Locate and identify every blood parasite.
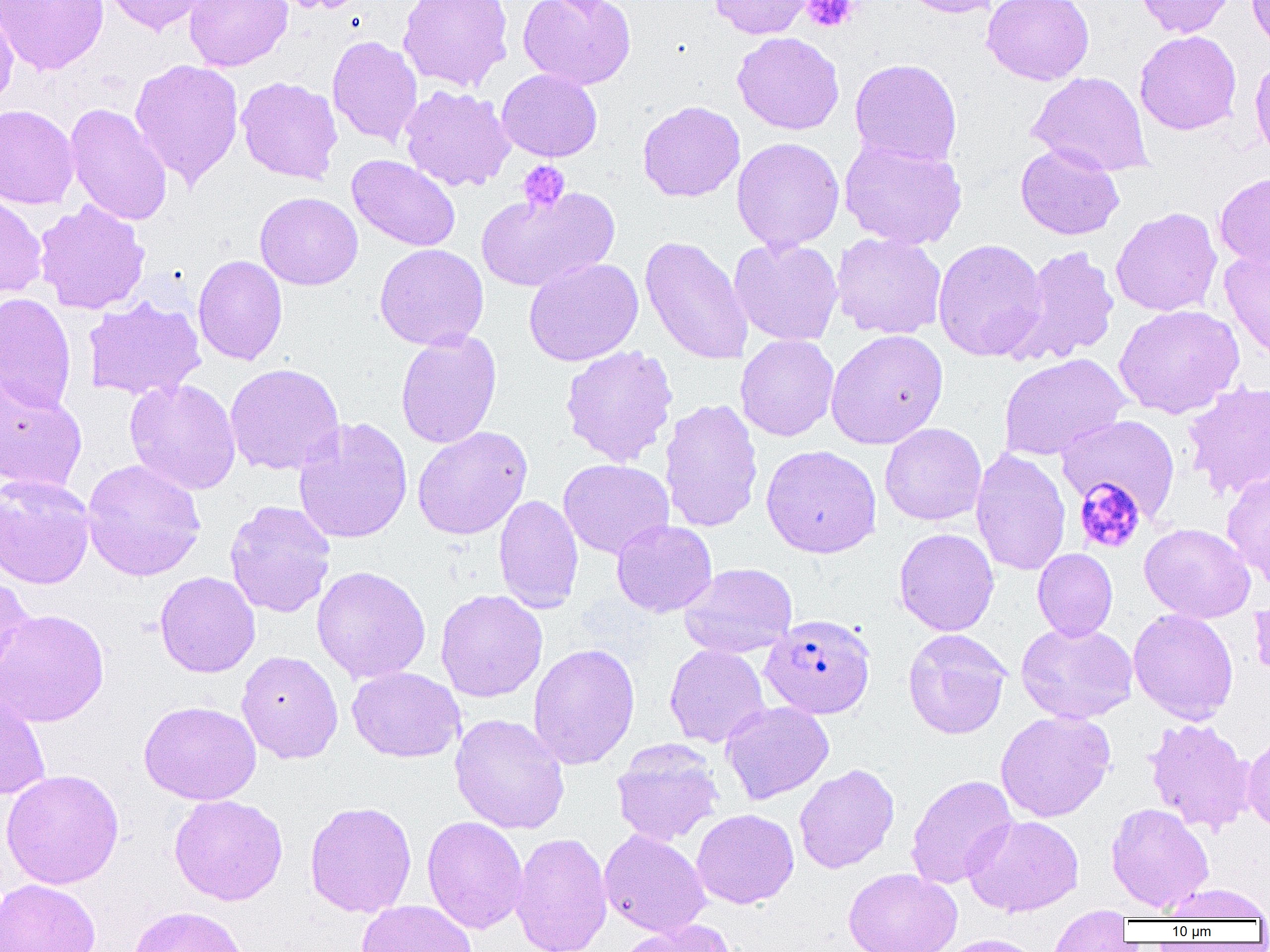

Approximate bounding boxes as (x1, y1, x2, y2) in pixels.
Plasmodium falciparum-infected red blood cells: (761, 613, 876, 719).
No Plasmodium ovale, Plasmodium malariae, Plasmodium vivax, Babesia divergens, or Trypanosoma brucei observed.

Platelet locations: (801, 0, 860, 32), (517, 160, 570, 212), (1074, 478, 1145, 553). Uninfected red blood cell locations: (0, 0, 109, 75), (101, 0, 213, 36), (184, 0, 292, 71), (270, 0, 371, 14), (398, 0, 513, 92), (518, 0, 636, 90), (708, 0, 815, 39), (896, 0, 1005, 18), (982, 0, 1094, 85), (1132, 0, 1237, 38), (1247, 0, 1270, 56), (0, 6, 18, 113), (1134, 30, 1242, 135), (733, 32, 845, 135), (327, 35, 422, 146), (1250, 55, 1270, 165), (129, 58, 244, 188), (849, 58, 963, 167), (496, 68, 602, 162), (1027, 71, 1153, 176), (236, 76, 343, 184), (400, 85, 515, 192), (637, 100, 745, 202), (65, 103, 172, 226), (0, 104, 79, 209), (731, 137, 845, 253), (839, 138, 968, 250), (1015, 143, 1124, 240), (347, 154, 460, 252), (1215, 172, 1270, 270), (476, 186, 619, 292), (0, 191, 47, 301), (254, 191, 363, 290), (34, 200, 151, 315), (1111, 207, 1222, 316), (832, 232, 947, 339), (640, 235, 754, 365), (728, 237, 843, 347), (932, 238, 1047, 362), (374, 243, 489, 351), (1011, 245, 1120, 365), (1220, 248, 1270, 363), (193, 254, 288, 366), (523, 257, 644, 367), (0, 292, 77, 413), (82, 295, 206, 400), (1113, 304, 1244, 419), (825, 329, 948, 450), (395, 330, 502, 449), (735, 334, 839, 441), (559, 345, 679, 467), (998, 353, 1131, 461), (224, 363, 345, 476), (0, 371, 87, 495), (124, 378, 242, 495), (1181, 380, 1270, 500), (659, 399, 764, 533), (1057, 415, 1180, 519), (293, 417, 413, 545), (879, 423, 987, 526), (412, 426, 532, 540), (760, 444, 882, 558), (970, 448, 1071, 576), (81, 459, 206, 581), (558, 459, 674, 559), (1221, 469, 1270, 588), (0, 474, 96, 590), (493, 493, 583, 613), (224, 500, 336, 618), (611, 520, 717, 617), (1139, 522, 1255, 623), (894, 527, 999, 636), (1032, 548, 1118, 641), (678, 563, 797, 659), (311, 565, 431, 684), (154, 571, 260, 678), (0, 573, 34, 688), (435, 589, 548, 703), (1250, 594, 1270, 682), (0, 608, 109, 728), (1128, 609, 1239, 724), (1016, 621, 1138, 724), (902, 628, 1011, 739), (528, 642, 640, 770), (664, 643, 771, 748), (236, 650, 343, 764), (347, 666, 465, 762), (0, 690, 51, 800), (138, 700, 261, 805), (720, 701, 834, 805), (995, 710, 1115, 822), (449, 713, 570, 834), (1144, 717, 1255, 835), (1243, 732, 1270, 834), (612, 740, 724, 846), (794, 763, 899, 874), (0, 768, 124, 889), (906, 774, 1018, 889), (168, 794, 288, 905), (304, 801, 417, 917), (1106, 802, 1214, 912), (692, 808, 799, 909), (963, 814, 1084, 917), (422, 816, 528, 935), (599, 829, 711, 938), (511, 831, 613, 952), (843, 867, 962, 952), (0, 879, 101, 952), (1162, 883, 1270, 921), (356, 900, 477, 952), (128, 905, 249, 952), (1048, 907, 1133, 951), (617, 920, 738, 952), (931, 934, 1047, 952). Slide-level diagnosis: Plasmodium falciparum. One field of a larger specimen. Light microscopy. Thin blood smear. Image is 1270×952 pixels. Captured at 1000x magnification.